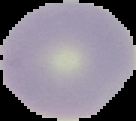

Summary:
  - Preparation: thin blood smear
  - Image size: 136×121 pixels
  - Result: negative for Plasmodium parasites
  - Image type: segmented cell region with the area outside set to black